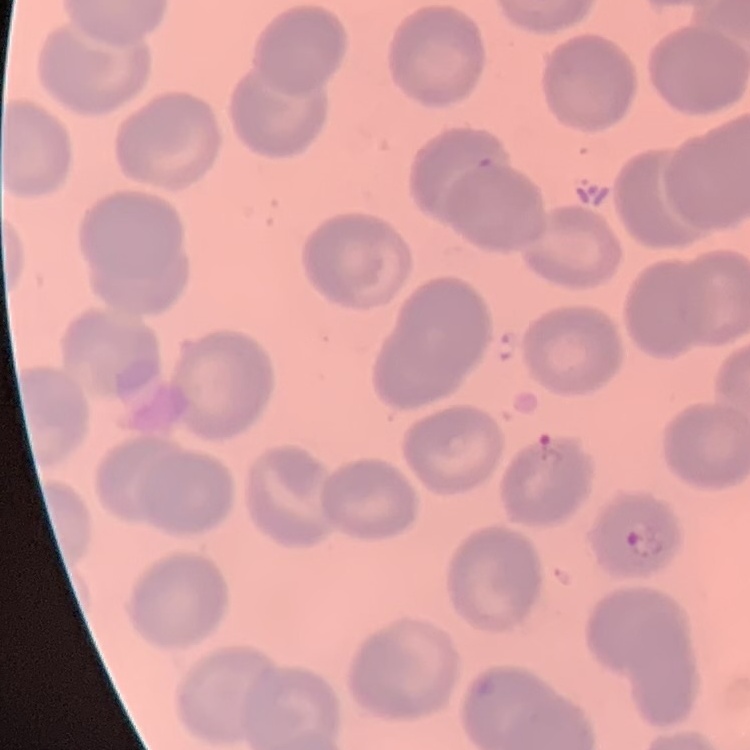
The erythrocytes show no rouleaux formation. Thin peripheral smear. Square crop of a larger photomicrograph. Field's or Giemsa stain.